Assess for malaria.
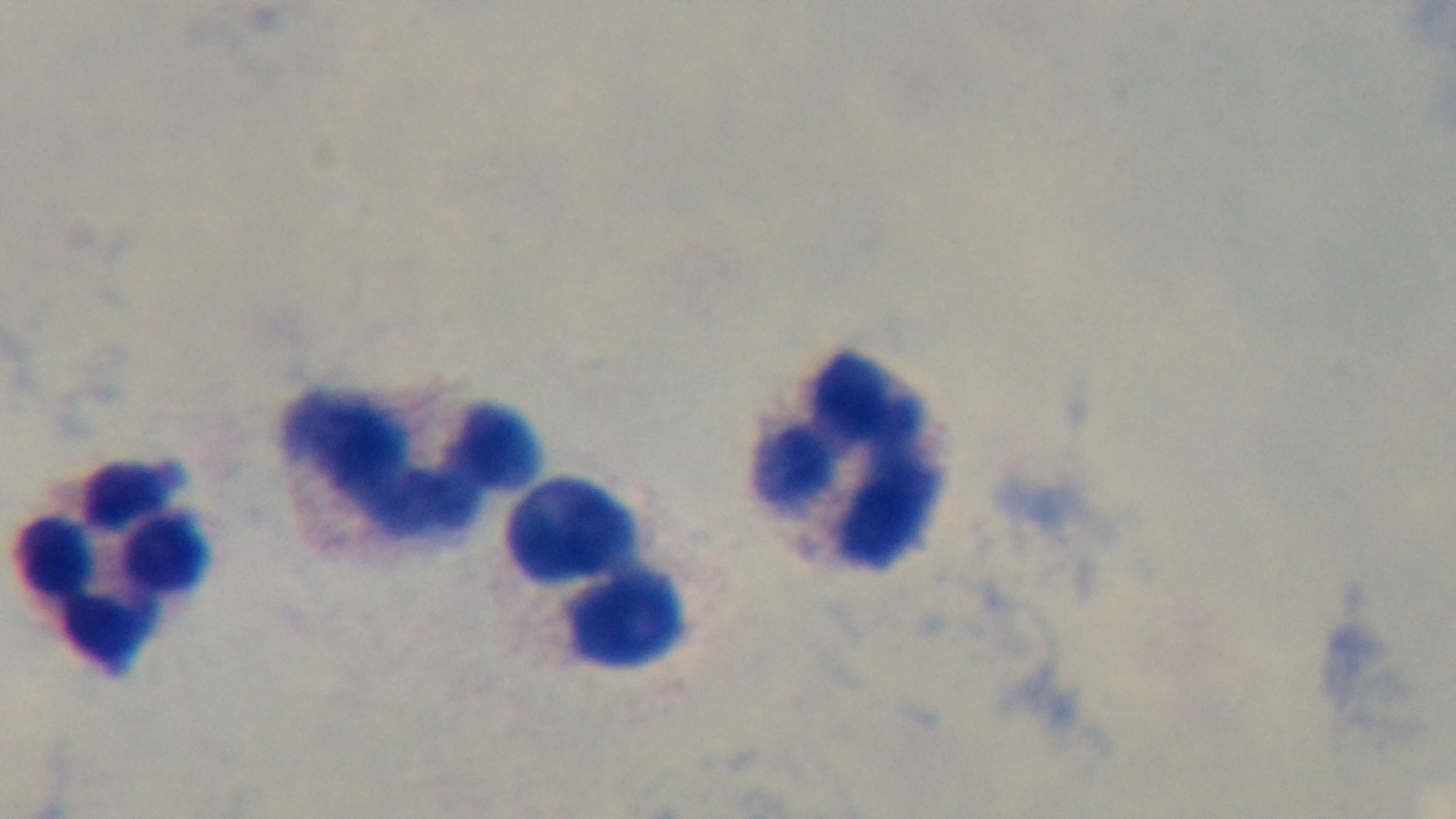

It is uninfected.

{
  "preparation": "thick smear",
  "stain": "Giemsa",
  "modality": "light microscopy",
  "capture": "mounted 4K digital camera",
  "field_of_view": "one from the slide",
  "objective": "100x oil immersion"
}